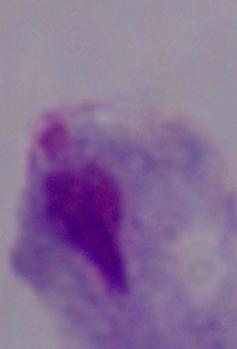

Photomicrograph. Captured at 1000x magnification. A trichomonad is seen.